Point out each Plasmodium parasite.
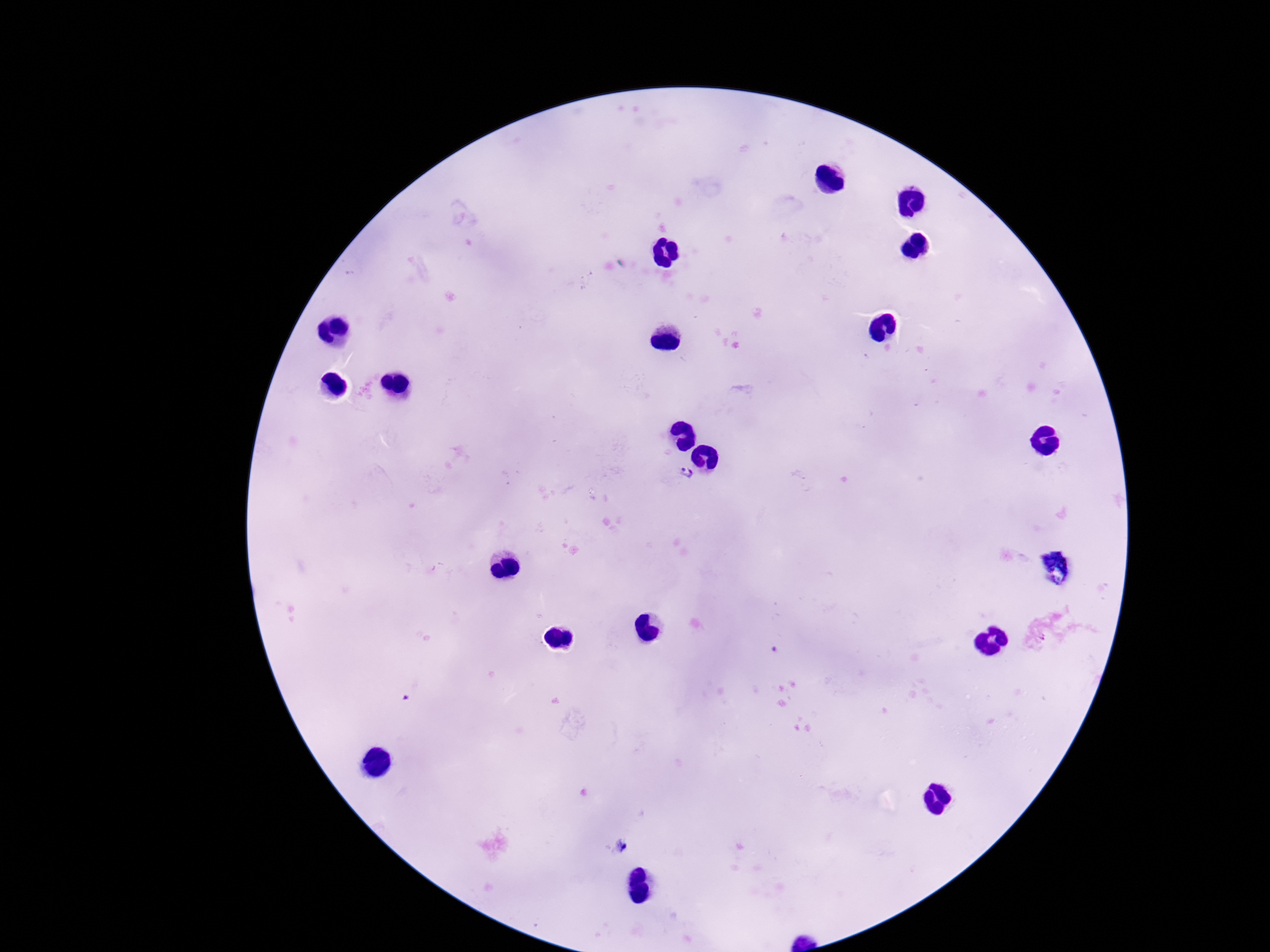
Approximate object centers, in pixels from the top-left corner.
Plasmodium parasites: (x=685, y=472).

field of view = one from this slide
patient malaria status = positive
preparation = thick peripheral-blood smear
magnification = 100x
image size = 1270×952 pixels
capture = smartphone camera through the microscope eyepiece
stain = Giemsa